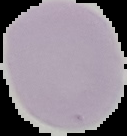

image size = 127×136 pixels
malaria status = uninfected
image type = segmented cell region with the area outside set to black
preparation = thin blood smear